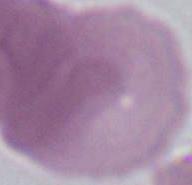
Captured at 1000x magnification. Micrograph. A red blood cell is seen.